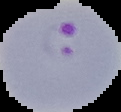
Image is 121×112 pixels. From a thin blood smear. Segmented cell region on a black background. Malaria status: parasitized.